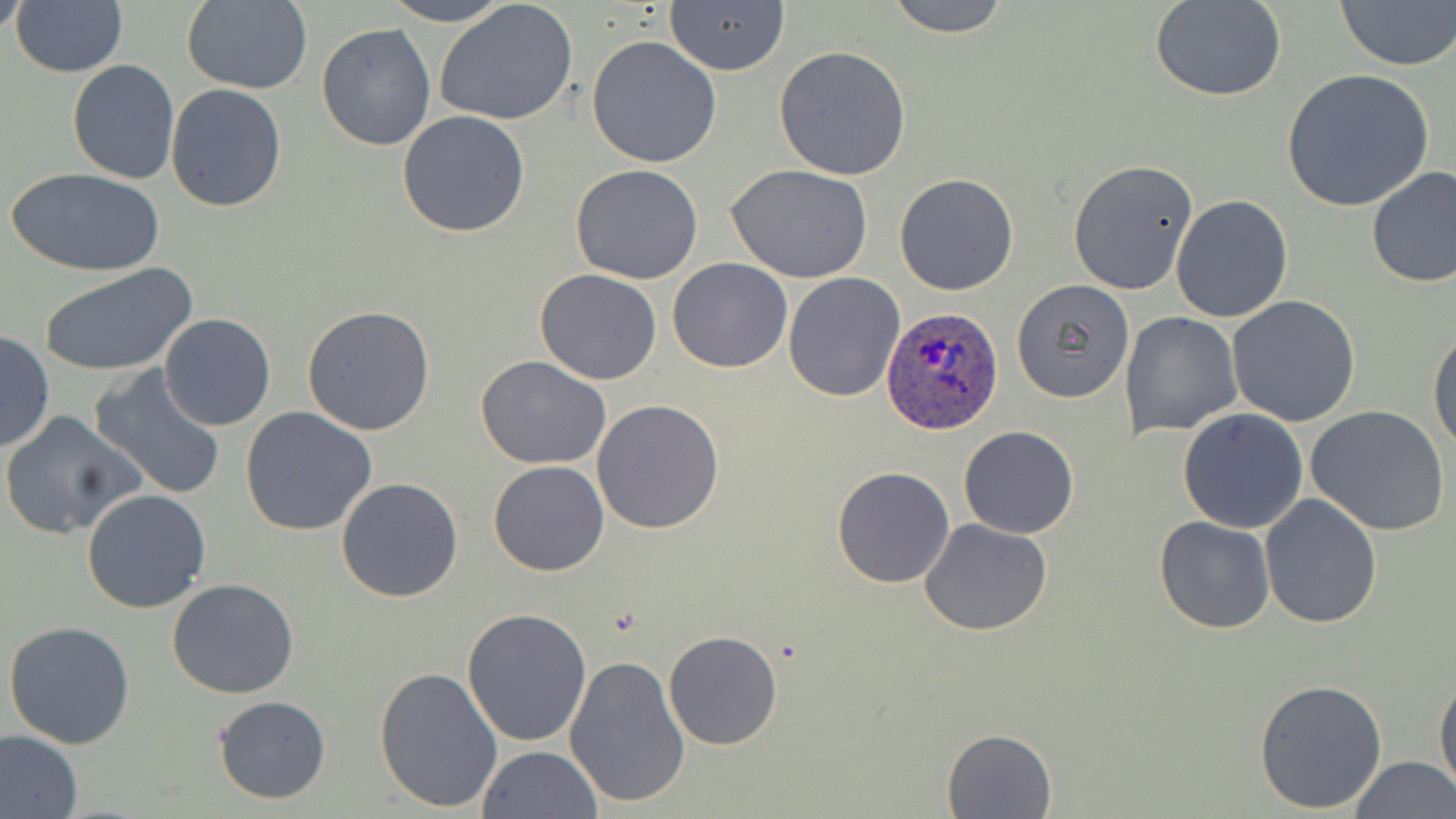

slide-level diagnosis = Plasmodium ovale
magnification = 1000x
image size = 1456×819 pixels
stain = May-Grünwald-Giemsa
modality = optical microscopy
uninfected red blood cell locations = approximate bounding boxes as named x1/y1/x2/y2 corners in pixels: (x1=1, y1=0, x2=30, y2=37), (x1=10, y1=0, x2=128, y2=77), (x1=181, y1=0, x2=313, y2=94), (x1=380, y1=0, x2=514, y2=26), (x1=881, y1=0, x2=1013, y2=36), (x1=1334, y1=0, x2=1456, y2=71), (x1=665, y1=1, x2=788, y2=74), (x1=1152, y1=1, x2=1286, y2=101), (x1=434, y1=2, x2=578, y2=126), (x1=316, y1=23, x2=437, y2=151), (x1=586, y1=37, x2=722, y2=168), (x1=772, y1=44, x2=913, y2=180), (x1=68, y1=59, x2=179, y2=184), (x1=1281, y1=69, x2=1435, y2=213), (x1=166, y1=84, x2=286, y2=211), (x1=397, y1=111, x2=531, y2=238), (x1=1066, y1=160, x2=1198, y2=294), (x1=725, y1=163, x2=873, y2=283), (x1=571, y1=164, x2=704, y2=284), (x1=1365, y1=164, x2=1456, y2=290), (x1=10, y1=167, x2=164, y2=277), (x1=894, y1=173, x2=1019, y2=295), (x1=1171, y1=194, x2=1293, y2=322), (x1=666, y1=258, x2=794, y2=373), (x1=38, y1=263, x2=198, y2=377), (x1=534, y1=269, x2=662, y2=385), (x1=782, y1=272, x2=905, y2=402), (x1=1012, y1=279, x2=1135, y2=403), (x1=1227, y1=295, x2=1362, y2=427), (x1=301, y1=304, x2=436, y2=435), (x1=1120, y1=311, x2=1242, y2=438), (x1=158, y1=312, x2=278, y2=430), (x1=1428, y1=325, x2=1456, y2=455), (x1=0, y1=330, x2=55, y2=451), (x1=476, y1=355, x2=613, y2=470), (x1=89, y1=365, x2=228, y2=502), (x1=592, y1=399, x2=726, y2=536), (x1=1306, y1=405, x2=1450, y2=536), (x1=241, y1=407, x2=378, y2=537), (x1=1177, y1=408, x2=1308, y2=533), (x1=1, y1=411, x2=145, y2=540), (x1=957, y1=424, x2=1076, y2=538), (x1=487, y1=460, x2=608, y2=577), (x1=832, y1=466, x2=957, y2=587), (x1=335, y1=476, x2=464, y2=603), (x1=80, y1=488, x2=212, y2=614), (x1=1259, y1=494, x2=1382, y2=629), (x1=1154, y1=517, x2=1276, y2=635), (x1=919, y1=518, x2=1054, y2=636), (x1=167, y1=577, x2=299, y2=699), (x1=462, y1=607, x2=593, y2=745), (x1=3, y1=621, x2=136, y2=749), (x1=664, y1=630, x2=782, y2=750), (x1=564, y1=652, x2=691, y2=809), (x1=375, y1=663, x2=502, y2=812), (x1=1434, y1=674, x2=1455, y2=799), (x1=1254, y1=678, x2=1387, y2=814), (x1=212, y1=695, x2=332, y2=804), (x1=943, y1=728, x2=1056, y2=817), (x1=0, y1=729, x2=84, y2=819), (x1=478, y1=745, x2=603, y2=819), (x1=1350, y1=756, x2=1455, y2=819)
Plasmodium ovale-infected red blood cell locations = approximate bounding boxes as named x1/y1/x2/y2 corners in pixels: (x1=881, y1=306, x2=1001, y2=434)
preparation = thin blood smear
field of view = one of a larger specimen